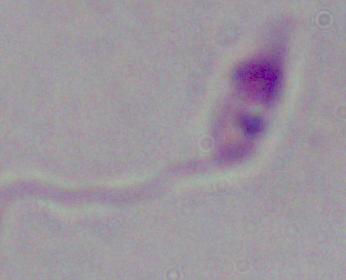

A Leishmania parasite is shown. Photomicrograph. 1000x magnification.